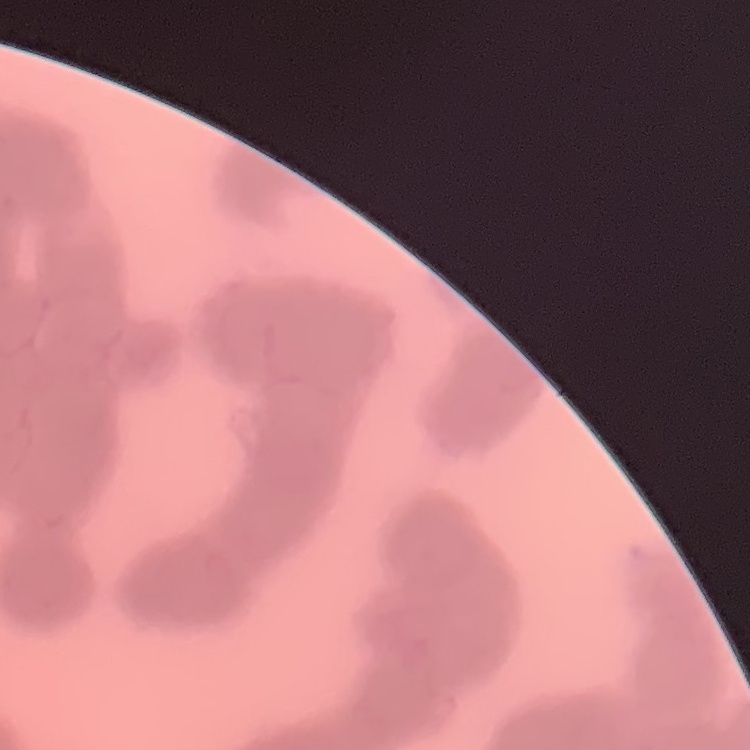
The red blood cells show rouleaux formation. Field's or Giemsa stain. Square crop of a larger photomicrograph. Thin peripheral smear.